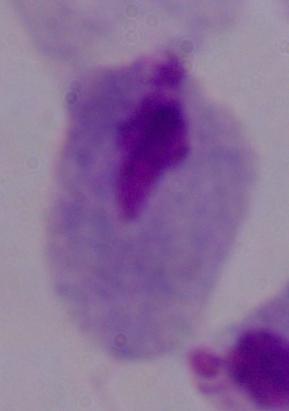 Photomicrograph. Captured at 1000x magnification. A trichomonad is seen.